Give the preparation type.
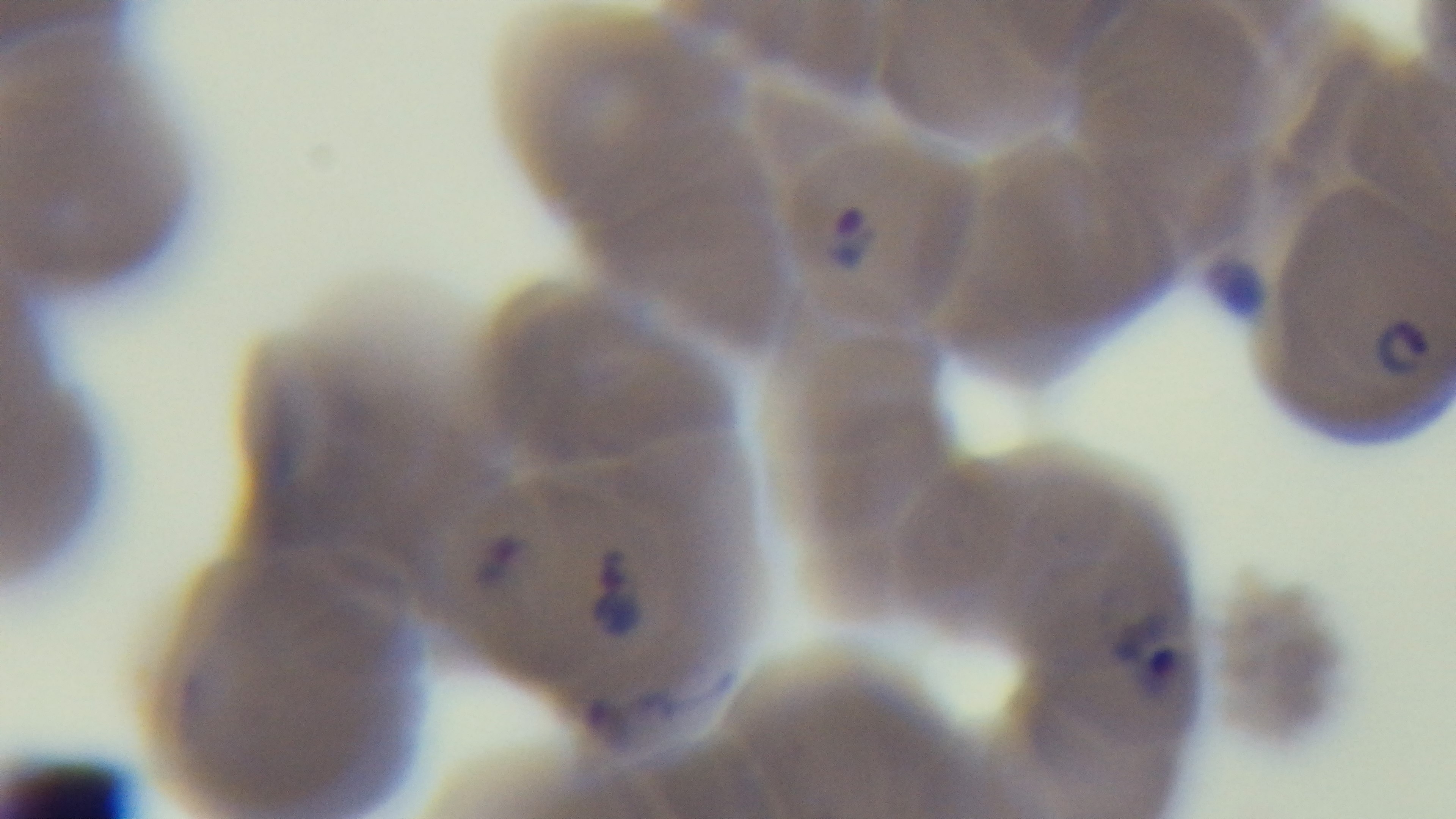

A thin smear.

malaria status = infected
field of view = one from the slide
stain = Giemsa
modality = light microscopy
objective = 100x oil immersion
capture = mounted 4K digital camera